Identify the parasite.
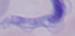

This is a trypanosome.

Captured at 1000x magnification. Photomicrograph.